Name the cell type shown.
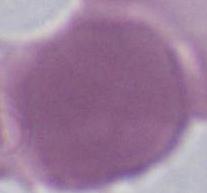

An erythrocyte.

modality = photomicrograph
magnification = 1000x